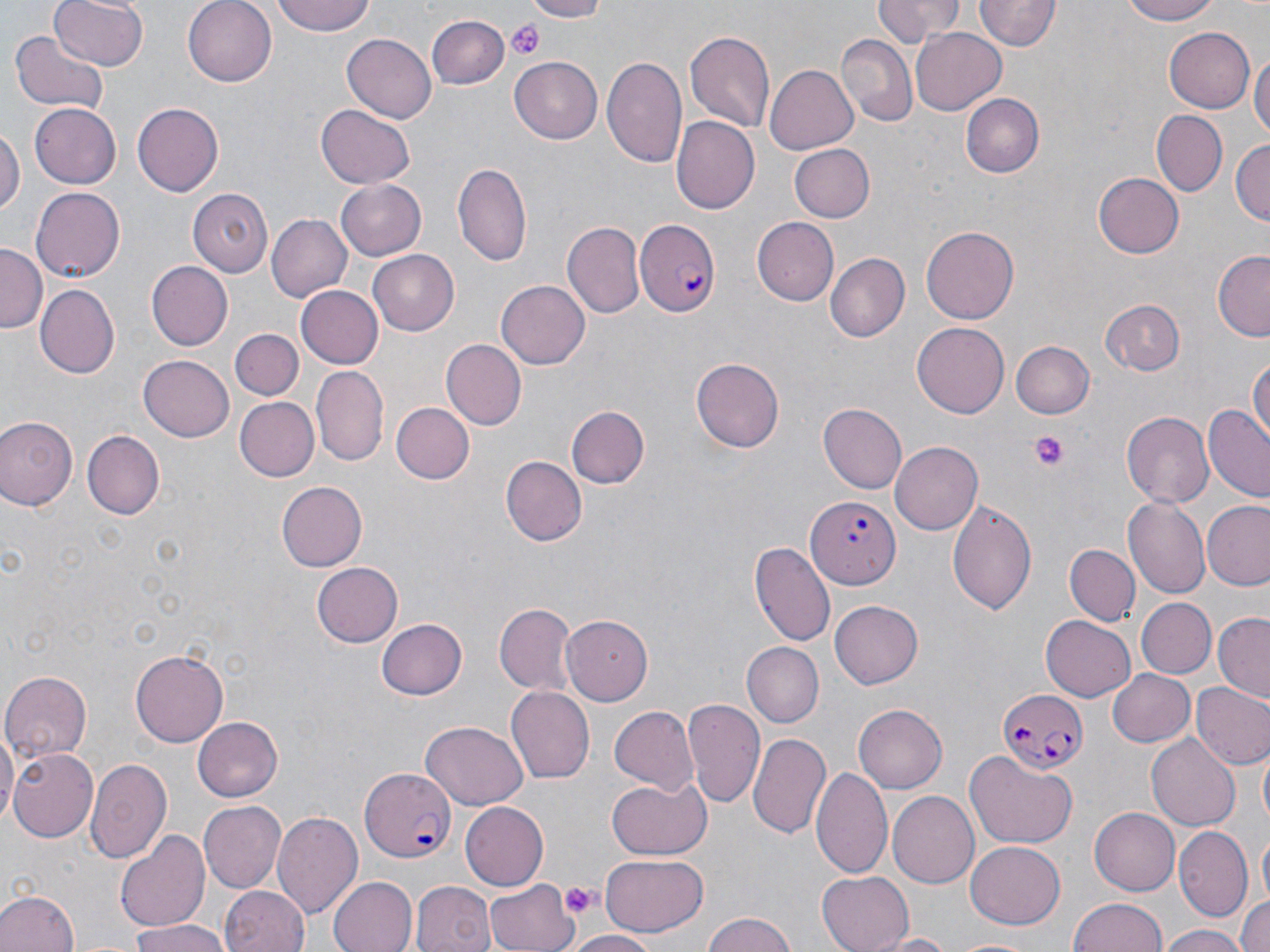
Summary:
  - Coordinate format: approximate bounding boxes as [x1, y1, x2, y2] in pixels
  - Platelet locations: [509, 21, 544, 59], [1028, 430, 1071, 472], [559, 883, 599, 916]
  - Uninfected red blood cell locations: [49, 0, 148, 72], [182, 0, 277, 85], [272, 0, 377, 38], [514, 0, 612, 20], [870, 0, 966, 44], [1117, 0, 1225, 25], [974, 1, 1058, 52], [428, 14, 509, 90], [1166, 25, 1256, 113], [911, 28, 1008, 115], [685, 29, 776, 131], [9, 30, 107, 116], [341, 32, 436, 121], [838, 35, 918, 127], [1249, 49, 1269, 147], [601, 51, 688, 168], [510, 54, 605, 144], [766, 67, 858, 153], [963, 94, 1043, 178], [29, 102, 121, 188], [132, 102, 223, 195], [315, 104, 415, 189], [1152, 111, 1226, 196], [673, 116, 761, 213], [0, 125, 22, 219], [1232, 138, 1269, 228], [788, 143, 875, 221], [455, 163, 532, 266], [1093, 172, 1184, 259], [333, 180, 428, 261], [30, 188, 124, 282], [188, 189, 272, 276], [265, 214, 352, 303], [755, 217, 839, 305], [564, 221, 643, 318], [923, 225, 1021, 324], [0, 245, 46, 331], [368, 249, 460, 336], [1213, 249, 1270, 342], [825, 253, 909, 342], [147, 261, 232, 350], [496, 279, 591, 371], [294, 284, 385, 370], [34, 285, 118, 377], [1101, 298, 1185, 376], [912, 322, 1009, 417], [229, 329, 302, 401], [442, 340, 526, 429], [1010, 341, 1094, 419], [1250, 352, 1269, 444], [138, 353, 234, 440], [691, 358, 782, 452], [303, 359, 383, 550], [312, 367, 388, 466], [233, 397, 319, 482], [392, 403, 474, 484], [818, 404, 907, 493], [567, 406, 649, 487], [1204, 407, 1270, 500], [1120, 408, 1213, 505], [0, 416, 78, 511], [81, 431, 163, 520], [892, 442, 983, 534], [502, 456, 585, 546], [276, 481, 367, 570], [1123, 497, 1210, 601], [945, 498, 1038, 615], [1203, 502, 1270, 591], [751, 541, 837, 645], [1063, 543, 1139, 625], [311, 561, 402, 647], [829, 600, 923, 689], [1138, 600, 1214, 678], [495, 603, 575, 693], [1212, 612, 1270, 703], [562, 613, 656, 704], [1040, 615, 1134, 702], [375, 617, 466, 699], [741, 643, 823, 729], [131, 649, 228, 746], [1106, 667, 1195, 747], [1, 671, 92, 761], [1190, 681, 1270, 771], [505, 685, 594, 783], [682, 697, 766, 809], [853, 703, 946, 793], [609, 705, 700, 794], [193, 716, 284, 802], [421, 721, 529, 808], [0, 723, 16, 826], [748, 734, 830, 843], [1148, 734, 1240, 831], [10, 748, 99, 841], [964, 750, 1080, 848], [1259, 751, 1269, 832], [85, 757, 172, 864], [810, 766, 892, 881], [607, 775, 710, 860], [886, 792, 977, 888], [199, 800, 285, 892], [459, 800, 549, 891], [1088, 807, 1179, 896], [273, 810, 365, 919], [1175, 824, 1252, 919], [115, 829, 211, 934], [1257, 831, 1270, 913], [963, 841, 1065, 930], [600, 854, 707, 936], [816, 871, 912, 952], [327, 876, 416, 952], [485, 876, 578, 952], [411, 880, 495, 952], [218, 885, 310, 952], [0, 889, 78, 952], [1236, 892, 1270, 952], [1069, 897, 1169, 952], [1194, 912, 1270, 952], [701, 913, 802, 952], [129, 923, 230, 952], [1159, 924, 1246, 952], [565, 930, 662, 952], [873, 933, 960, 951], [950, 937, 1042, 952]
  - Plasmodium falciparum-infected red blood cell locations: [634, 218, 718, 319], [806, 495, 897, 586], [996, 687, 1086, 777], [358, 769, 456, 864]
  - Slide-level diagnosis: Plasmodium falciparum
  - Image size: 1270×952 pixels
  - Modality: light microscopy
  - Stain: May-Grünwald-Giemsa
  - Field of view: single
  - Preparation: thin blood smear
  - Magnification: 1000x